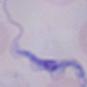

Summary:
  - Magnification: 1000x
  - Identification: trypanosome
  - Modality: micrograph